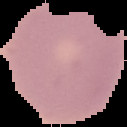

preparation = thin blood film
image size = 127×127 pixels
malaria status = uninfected
image type = segmented cell region on a black background